Report the malaria status of this cell.
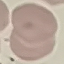
Uninfected.

Acquired by smartphone through the microscope eyepiece. Giemsa stain. Thin smear of blood. Cell patch, automatically extracted from a larger field of view and resized to 64 × 64 pixels.